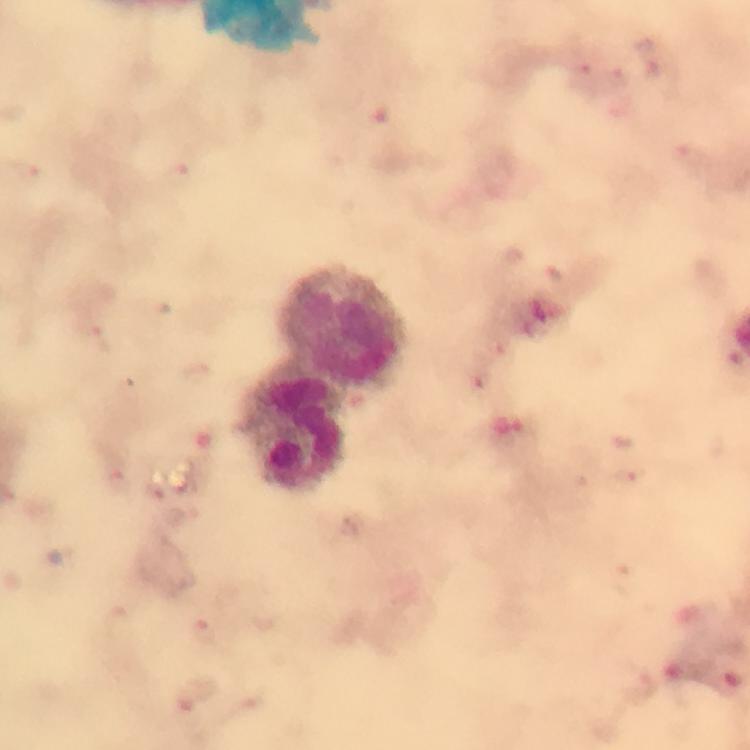
leukocyte locations = approximate centers as (x, y) in pixels: (343, 325), (295, 425)
context = from a malaria diagnostic workup
magnification = 100x
image size = 750×750 pixels
preparation = thick blood film
immersion oil = applied
stain = Giemsa
cropped from = a single field of view
capture = smartphone camera through the microscope
Plasmodium parasite locations = approximate centers as (x, y) in pixels: (616, 78), (177, 174), (104, 338), (629, 472)